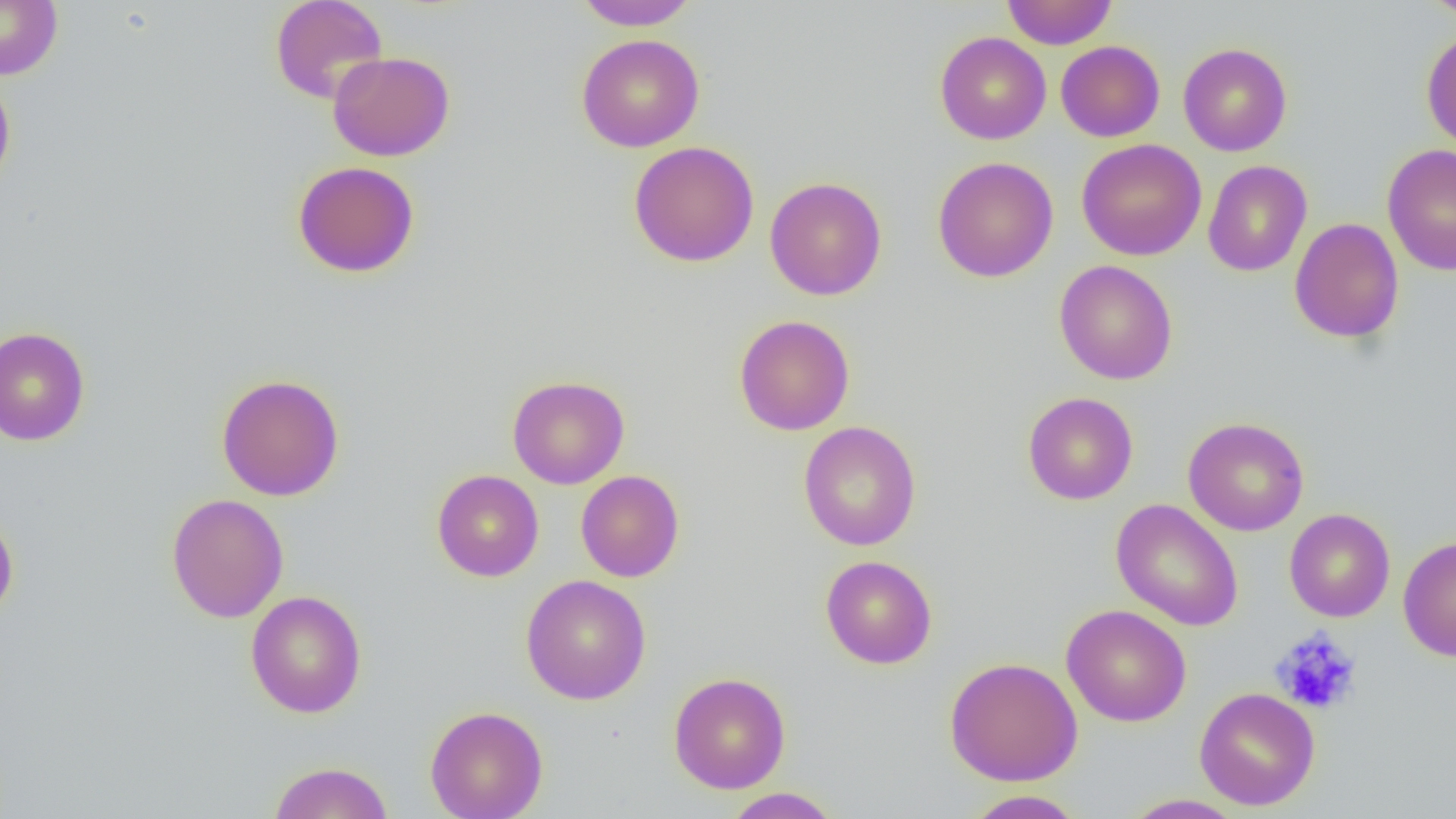

slide_level_diagnosis: negative for blood parasites
platelet_locations: 'approximate bounding boxes as (x1, y1, x2, y2) in pixels: (1269, 627, 1362, 715)'
image_size: 1456×819 pixels
preparation: thin blood film
magnification: 1000x
field_of_view: single
modality: light microscopy
uninfected_red_blood_cell_locations: 'approximate bounding boxes as (x1, y1, x2, y2) in pixels: (0, 0, 63, 80), (269, 0, 389, 104), (573, 0, 699, 31), (1002, 0, 1118, 49), (1423, 0, 1456, 21), (1421, 27, 1456, 151), (935, 31, 1051, 145), (576, 33, 705, 152), (1055, 40, 1165, 142), (1178, 43, 1292, 156), (328, 51, 455, 161), (0, 73, 16, 193), (1076, 139, 1206, 261), (628, 140, 759, 267), (1382, 143, 1456, 275), (932, 156, 1059, 283), (1202, 159, 1313, 277), (292, 160, 420, 278), (765, 176, 887, 301), (1289, 217, 1404, 344), (1054, 259, 1178, 385), (733, 315, 855, 435), (0, 326, 91, 446), (216, 373, 345, 501), (507, 375, 630, 489), (1023, 392, 1138, 505), (1183, 416, 1309, 536), (798, 421, 921, 551), (431, 469, 544, 582), (576, 470, 685, 582), (166, 493, 289, 623), (1111, 499, 1244, 632), (0, 506, 19, 625), (1284, 508, 1395, 622), (1398, 535, 1456, 661), (820, 555, 937, 669), (520, 574, 651, 705), (245, 590, 367, 718), (1061, 604, 1192, 727), (944, 656, 1083, 786), (668, 672, 791, 794), (1195, 687, 1320, 811), (425, 705, 548, 819), (267, 761, 395, 819), (722, 787, 842, 818), (962, 789, 1087, 818), (1122, 794, 1247, 819)'